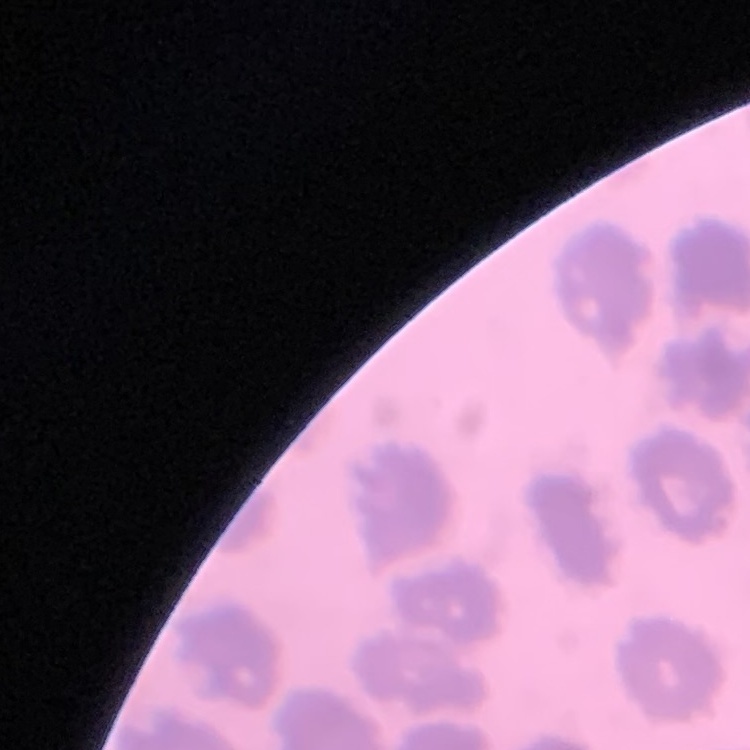

red blood cell morphology = no rouleaux formation
preparation = thin blood film
stain = Field's or Giemsa
image type = one tile cut from a larger photomicrograph